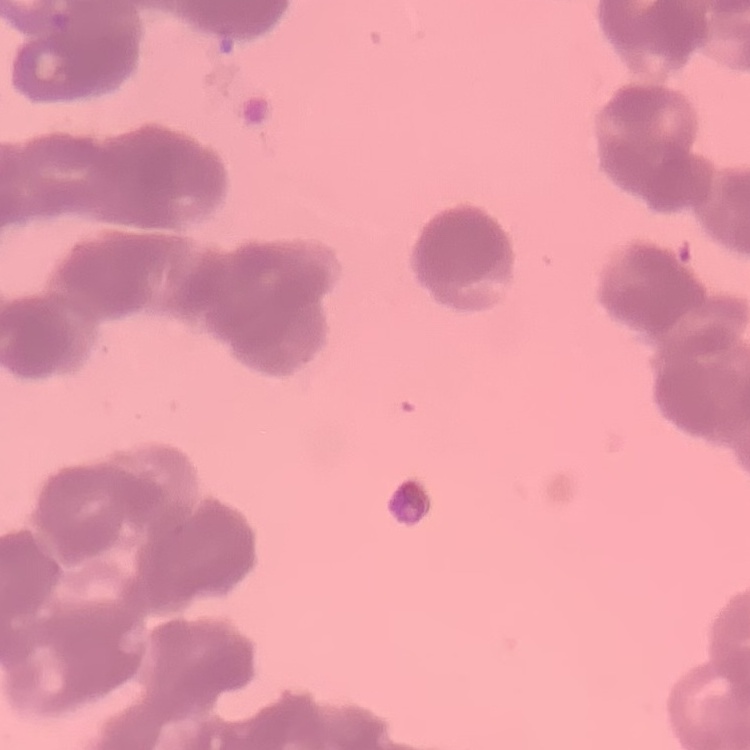 The erythrocytes show rouleaux formation. Field's or Giemsa stain. Thin blood smear. Square crop of a larger photomicrograph.